Outline each Plasmodium falciparum-infected red blood cell.
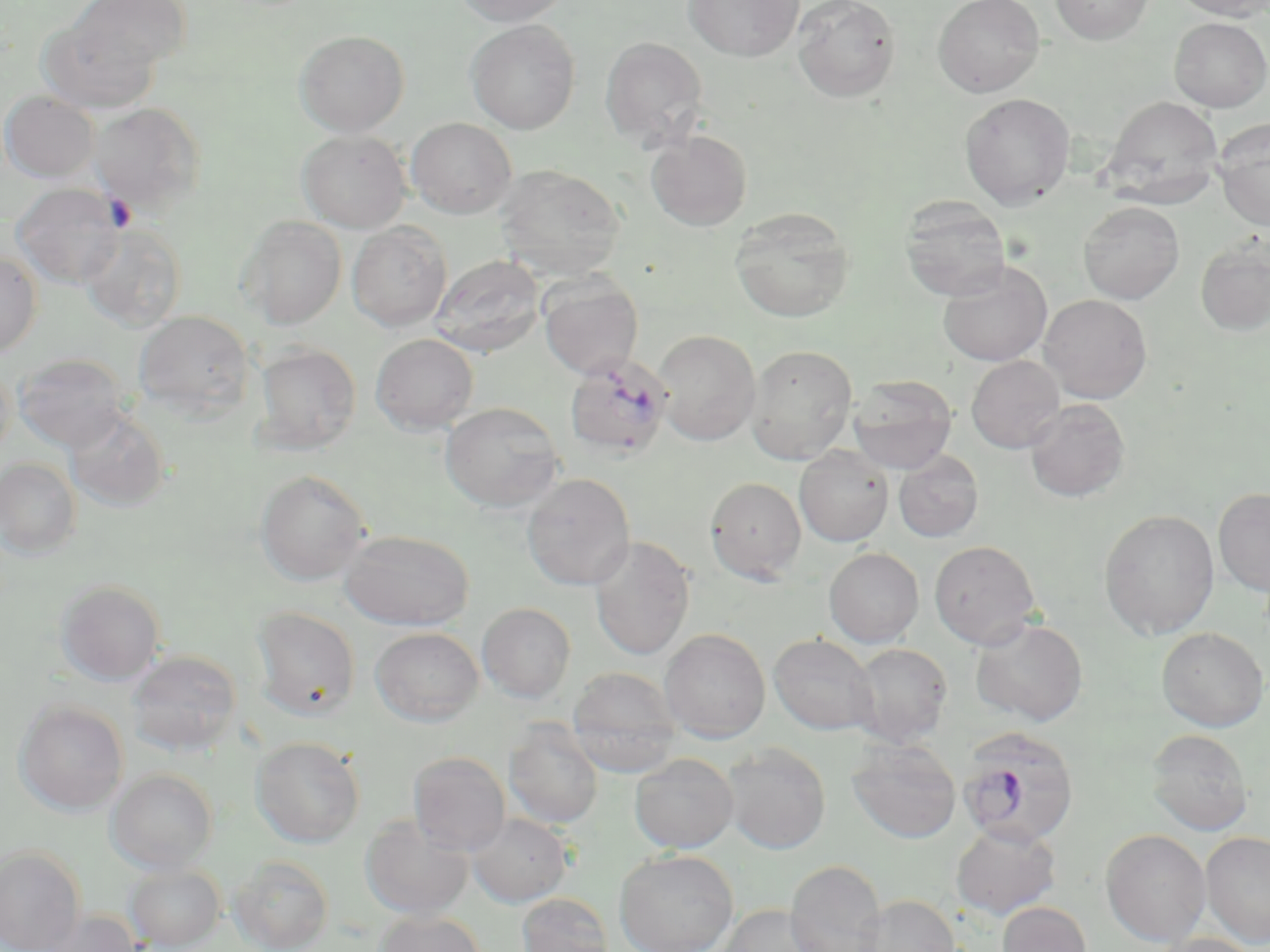
Approximate bounding boxes as (x1,y1)-(x2,y2) corner pairs in pixels.
Plasmodium falciparum-infected red blood cells: (563,353)-(674,460), (956,726)-(1080,848).

Uninfected red blood cell locations: (65,0)-(191,76), (453,0)-(572,27), (683,0)-(805,62), (792,0)-(901,103), (933,0)-(1045,98), (1050,0)-(1153,44), (1172,0)-(1270,20), (38,14)-(162,112), (1169,17)-(1270,112), (465,19)-(581,134), (294,29)-(409,136), (599,37)-(709,148), (0,90)-(99,182), (960,92)-(1076,210), (1102,96)-(1224,208), (90,102)-(205,212), (406,118)-(517,219), (1213,119)-(1270,231), (645,129)-(753,231), (297,130)-(411,233), (495,165)-(627,280), (12,183)-(125,288), (900,197)-(1011,301), (1078,201)-(1184,304), (730,207)-(855,323), (239,216)-(346,329), (79,223)-(188,333), (347,223)-(452,331), (1195,236)-(1270,336), (0,251)-(42,358), (429,254)-(545,358), (937,261)-(1052,366), (538,275)-(643,379), (1039,294)-(1153,402), (133,311)-(255,419), (653,329)-(760,445), (370,334)-(479,434), (253,343)-(362,453), (746,344)-(858,464), (14,352)-(130,452), (966,355)-(1065,453), (0,365)-(16,462), (847,375)-(958,474), (1024,399)-(1130,502), (440,402)-(564,512), (64,407)-(172,512), (794,445)-(893,547), (893,450)-(984,542), (0,458)-(82,559), (254,470)-(372,585), (521,473)-(635,590), (705,476)-(807,583), (1213,488)-(1270,596), (1099,510)-(1219,639), (339,529)-(474,630), (589,536)-(695,661), (929,540)-(1041,650), (823,547)-(924,648), (55,580)-(166,685), (477,602)-(576,703), (251,606)-(361,720), (970,618)-(1088,726), (370,627)-(483,726), (1157,627)-(1268,732), (659,628)-(770,743), (769,633)-(878,735), (849,643)-(953,747), (127,649)-(243,756), (568,667)-(681,776), (14,700)-(129,816), (504,719)-(603,829), (1146,728)-(1253,836), (251,736)-(365,848), (847,738)-(962,844), (721,742)-(831,854), (408,751)-(510,856), (629,753)-(738,853), (107,768)-(218,873), (467,812)-(572,907), (360,815)-(474,919), (950,821)-(1061,920), (1101,829)-(1211,947), (1201,831)-(1270,948), (0,846)-(86,952), (614,849)-(739,952), (229,855)-(335,952), (784,859)-(887,952), (124,862)-(226,951), (517,893)-(613,952), (856,895)-(962,952), (996,901)-(1092,952), (716,904)-(834,952), (39,909)-(143,952), (375,910)-(486,952), (1149,933)-(1265,952). Slide-level diagnosis: Plasmodium falciparum. Image is 1270×952 pixels. Light microscopy. Thin blood film. 1000x magnification. May-Grünwald-Giemsa-stained preparation. One field of a larger specimen.